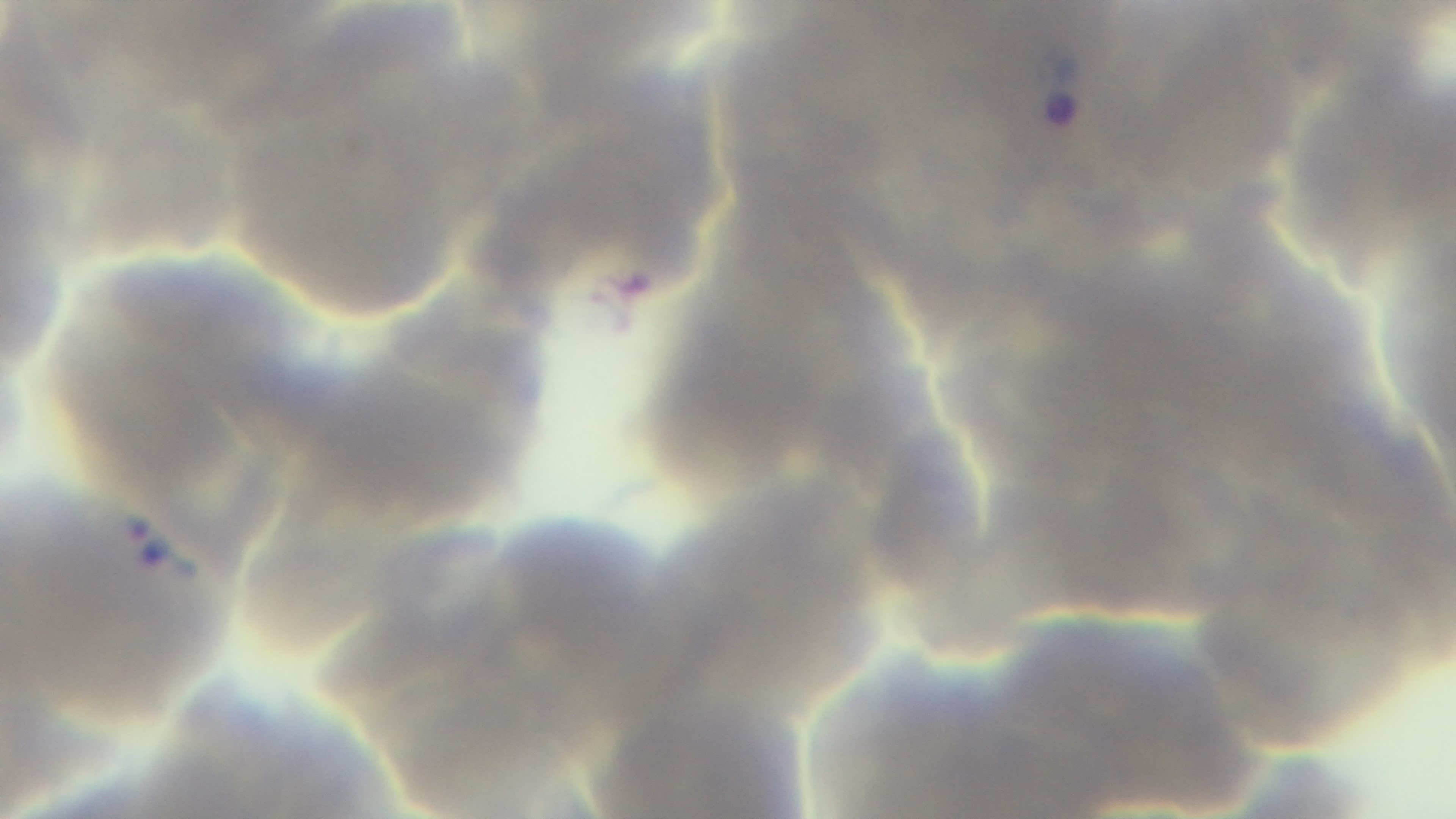
Captured with a mounted 4K digital camera. Single field of view. Malaria status: positive. 100x oil-immersion objective. Photomicrograph. Preparation: thin blood film. Giemsa stain.